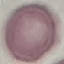
Result: negative for malaria parasites. Acquired by smartphone through the microscope eyepiece. Automatically extracted cell patch, resized to 64 × 64 pixels. Giemsa stain. Thin smear of blood.